State which cell type is depicted.
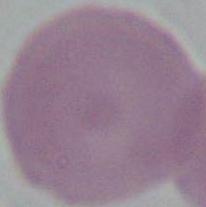
An erythrocyte.

1000x magnification. Photomicrograph.